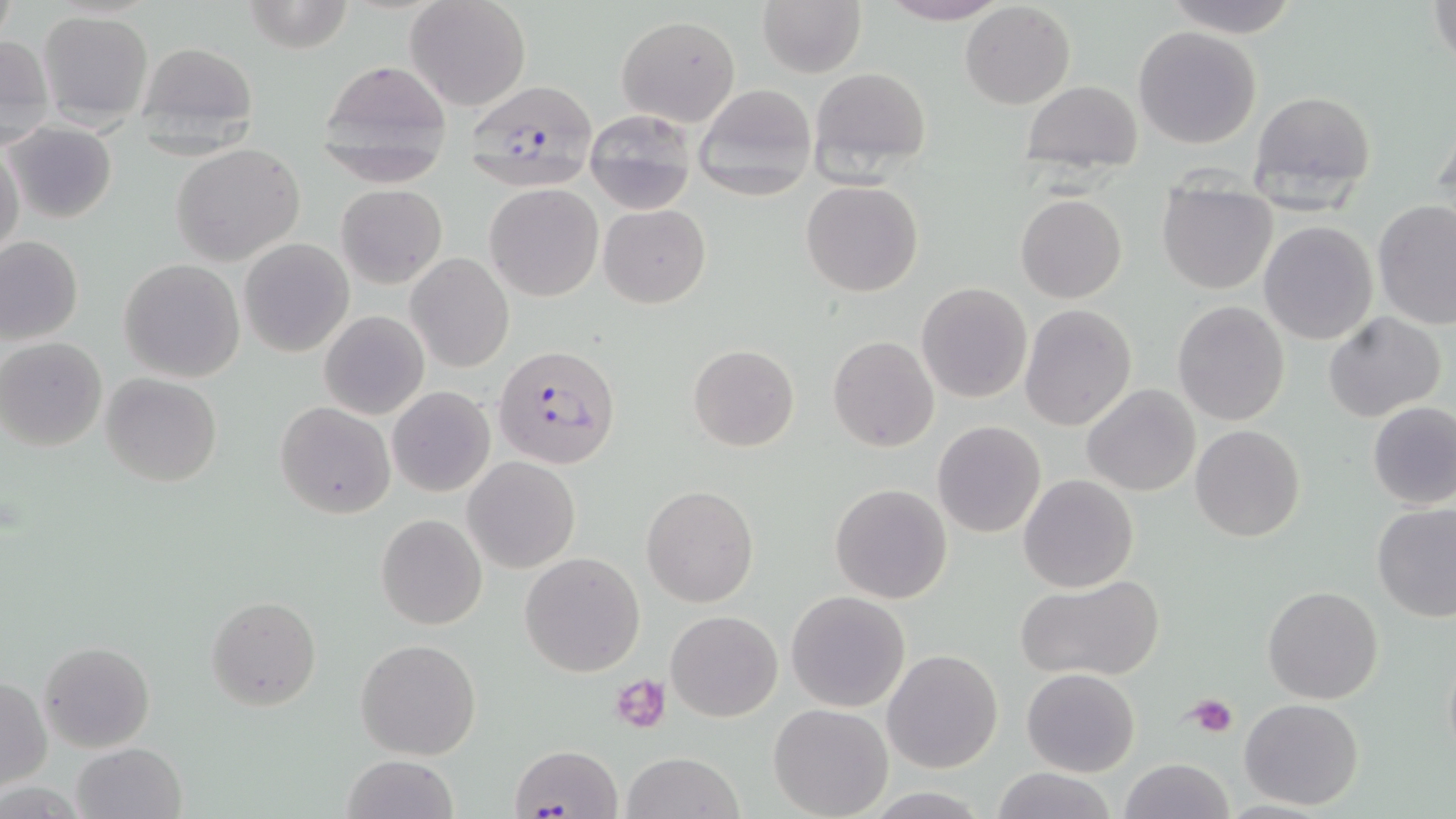 Approximate bounding boxes as named x1/y1/x2/y2 corners in pixels. Plasmodium falciparum-infected red blood cell locations: (x1=464, y1=80, x2=596, y2=172), (x1=491, y1=341, x2=620, y2=468). Uninfected red blood cell locations: (x1=243, y1=0, x2=354, y2=53), (x1=404, y1=0, x2=532, y2=112), (x1=876, y1=0, x2=1009, y2=26), (x1=1161, y1=0, x2=1300, y2=36), (x1=1429, y1=0, x2=1455, y2=69), (x1=758, y1=1, x2=866, y2=76), (x1=960, y1=2, x2=1075, y2=109), (x1=38, y1=9, x2=154, y2=127), (x1=615, y1=13, x2=741, y2=127), (x1=1133, y1=25, x2=1262, y2=150), (x1=0, y1=35, x2=54, y2=147), (x1=133, y1=40, x2=262, y2=146), (x1=316, y1=58, x2=453, y2=173), (x1=809, y1=66, x2=934, y2=182), (x1=1021, y1=80, x2=1143, y2=170), (x1=693, y1=84, x2=815, y2=201), (x1=1249, y1=89, x2=1377, y2=203), (x1=1431, y1=104, x2=1456, y2=210), (x1=585, y1=114, x2=695, y2=210), (x1=5, y1=122, x2=118, y2=223), (x1=0, y1=141, x2=25, y2=262), (x1=172, y1=142, x2=306, y2=266), (x1=802, y1=181, x2=923, y2=296), (x1=485, y1=183, x2=604, y2=301), (x1=336, y1=184, x2=447, y2=287), (x1=1157, y1=186, x2=1278, y2=295), (x1=1016, y1=194, x2=1127, y2=303), (x1=1373, y1=201, x2=1456, y2=332), (x1=598, y1=204, x2=711, y2=309), (x1=1259, y1=221, x2=1378, y2=346), (x1=1, y1=236, x2=83, y2=344), (x1=239, y1=238, x2=354, y2=357), (x1=408, y1=254, x2=514, y2=372), (x1=119, y1=259, x2=245, y2=382), (x1=916, y1=282, x2=1032, y2=403), (x1=1171, y1=301, x2=1290, y2=426), (x1=1020, y1=303, x2=1138, y2=430), (x1=320, y1=310, x2=429, y2=420), (x1=1324, y1=311, x2=1447, y2=423), (x1=0, y1=337, x2=107, y2=451), (x1=827, y1=337, x2=940, y2=453), (x1=687, y1=344, x2=800, y2=452), (x1=101, y1=374, x2=222, y2=487), (x1=388, y1=385, x2=495, y2=496), (x1=1082, y1=385, x2=1200, y2=496), (x1=1367, y1=401, x2=1456, y2=510), (x1=276, y1=402, x2=395, y2=518), (x1=933, y1=420, x2=1047, y2=538), (x1=1190, y1=425, x2=1306, y2=544), (x1=464, y1=458, x2=579, y2=573), (x1=1018, y1=475, x2=1139, y2=592), (x1=830, y1=483, x2=952, y2=604), (x1=642, y1=485, x2=758, y2=606), (x1=1372, y1=503, x2=1455, y2=622), (x1=377, y1=513, x2=487, y2=630), (x1=520, y1=551, x2=645, y2=677), (x1=1015, y1=576, x2=1165, y2=680), (x1=1263, y1=585, x2=1383, y2=703), (x1=785, y1=591, x2=912, y2=712), (x1=206, y1=596, x2=321, y2=710), (x1=665, y1=610, x2=783, y2=721), (x1=355, y1=638, x2=481, y2=759), (x1=39, y1=640, x2=155, y2=752), (x1=1441, y1=641, x2=1456, y2=775), (x1=882, y1=648, x2=1003, y2=773), (x1=1023, y1=668, x2=1140, y2=776), (x1=1, y1=677, x2=51, y2=791), (x1=1239, y1=697, x2=1365, y2=809), (x1=769, y1=703, x2=894, y2=818), (x1=71, y1=742, x2=186, y2=819), (x1=511, y1=743, x2=621, y2=816), (x1=622, y1=750, x2=742, y2=819), (x1=341, y1=754, x2=459, y2=819), (x1=1119, y1=758, x2=1235, y2=819), (x1=991, y1=767, x2=1116, y2=819). Platelet locations: (x1=611, y1=674, x2=673, y2=734), (x1=1186, y1=693, x2=1240, y2=737). Slide-level diagnosis: Plasmodium falciparum. Light microscopy. May-Grünwald-Giemsa-stained preparation. Image is 1456×819 pixels. 1000x magnification. Thin blood film. One field of a larger specimen.